Locate every malaria parasite.
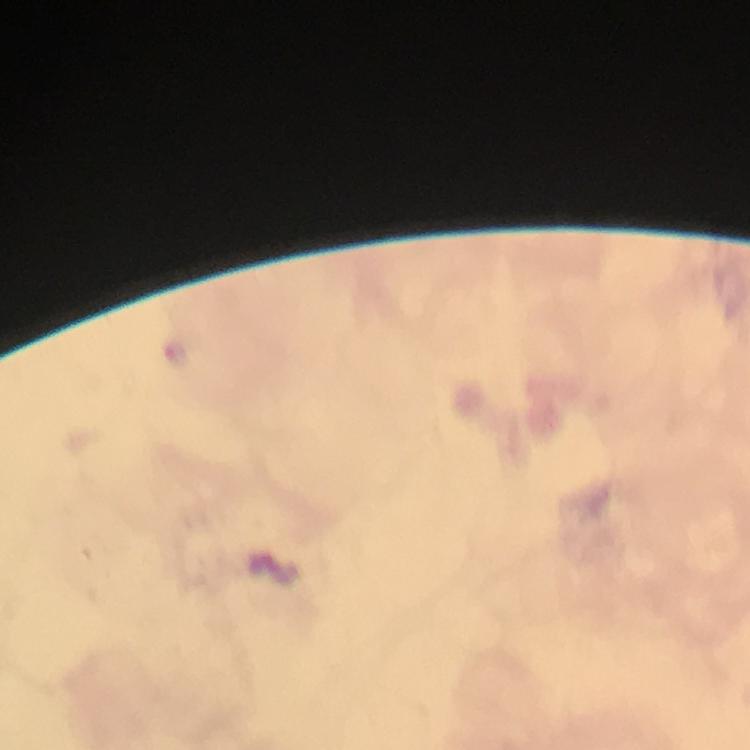
Approximate centers as [x, y] in pixels.
Malaria parasites: [178, 350].

Summary:
  - Stain: Giemsa
  - Magnification: 100x
  - Context: from a diagnostic examination for malaria
  - Capture: smartphone mounted on the microscope
  - Image size: 750×750 pixels
  - Immersion oil: applied
  - Preparation: thick blood smear
  - Cropped from: one field of view